Identify the cell.
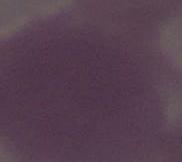

An erythrocyte.

Summary:
  - Modality: photomicrograph
  - Magnification: 1000x